Classify this cell by malaria status.
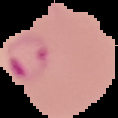

It is parasitized.

From a thin blood smear. The area outside the segmented cell region is set to black. Image is 118×118 pixels.